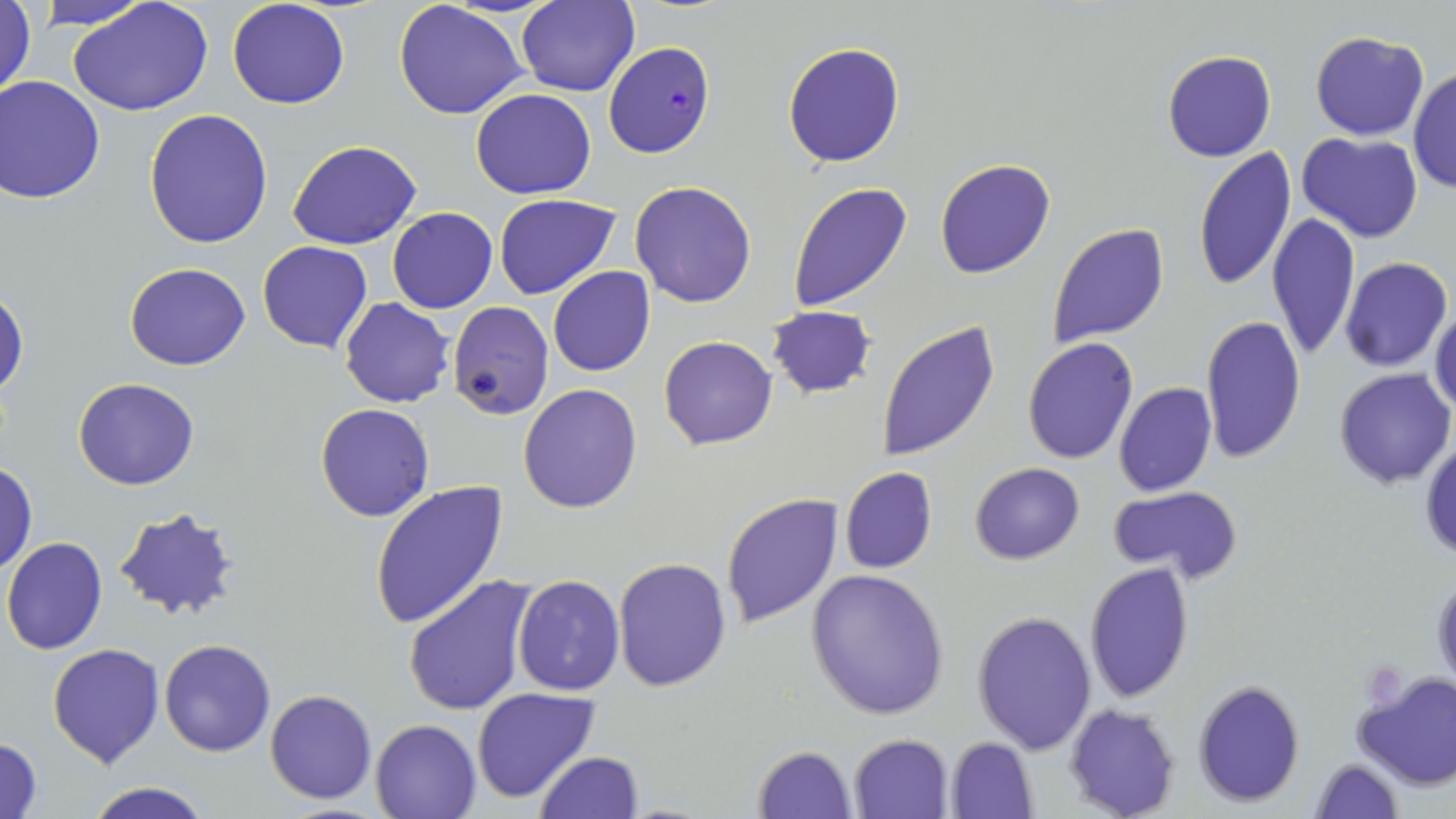
Summary:
  - Coordinate format: approximate bounding boxes as named x1/y1/x2/y2 corners in pixels
  - Uninfected red blood cell locations: (x1=29, y1=0, x2=155, y2=29), (x1=67, y1=1, x2=216, y2=117), (x1=226, y1=1, x2=351, y2=110), (x1=393, y1=1, x2=528, y2=120), (x1=515, y1=1, x2=638, y2=97), (x1=1, y1=2, x2=37, y2=103), (x1=1310, y1=31, x2=1427, y2=140), (x1=782, y1=42, x2=905, y2=167), (x1=1162, y1=50, x2=1276, y2=163), (x1=1410, y1=67, x2=1455, y2=195), (x1=0, y1=76, x2=106, y2=204), (x1=470, y1=88, x2=597, y2=199), (x1=142, y1=109, x2=274, y2=249), (x1=1297, y1=132, x2=1422, y2=241), (x1=289, y1=140, x2=421, y2=250), (x1=1193, y1=148, x2=1297, y2=292), (x1=935, y1=159, x2=1055, y2=279), (x1=629, y1=181, x2=757, y2=308), (x1=788, y1=182, x2=913, y2=314), (x1=494, y1=194, x2=620, y2=300), (x1=387, y1=207, x2=498, y2=313), (x1=1268, y1=212, x2=1360, y2=361), (x1=1047, y1=223, x2=1170, y2=348), (x1=256, y1=241, x2=373, y2=353), (x1=1339, y1=257, x2=1451, y2=372), (x1=125, y1=262, x2=251, y2=370), (x1=547, y1=265, x2=655, y2=377), (x1=0, y1=285, x2=26, y2=404), (x1=340, y1=297, x2=454, y2=408), (x1=765, y1=305, x2=878, y2=400), (x1=1429, y1=307, x2=1456, y2=416), (x1=1199, y1=316, x2=1307, y2=463), (x1=877, y1=321, x2=1002, y2=460), (x1=659, y1=335, x2=778, y2=450), (x1=1022, y1=336, x2=1139, y2=464), (x1=1334, y1=369, x2=1454, y2=489), (x1=74, y1=378, x2=200, y2=490), (x1=517, y1=383, x2=644, y2=515), (x1=1115, y1=383, x2=1217, y2=497), (x1=315, y1=403, x2=434, y2=521), (x1=1421, y1=436, x2=1456, y2=562), (x1=0, y1=460, x2=37, y2=576), (x1=970, y1=462, x2=1085, y2=563), (x1=840, y1=467, x2=937, y2=574), (x1=368, y1=479, x2=508, y2=630), (x1=1108, y1=486, x2=1245, y2=582), (x1=720, y1=493, x2=845, y2=631), (x1=113, y1=506, x2=244, y2=622), (x1=1, y1=537, x2=107, y2=655), (x1=612, y1=558, x2=732, y2=692), (x1=1083, y1=562, x2=1195, y2=704), (x1=805, y1=567, x2=952, y2=718), (x1=1432, y1=573, x2=1455, y2=694), (x1=403, y1=574, x2=537, y2=716), (x1=513, y1=575, x2=625, y2=695), (x1=972, y1=610, x2=1097, y2=754), (x1=158, y1=639, x2=276, y2=757), (x1=47, y1=643, x2=165, y2=767), (x1=1351, y1=668, x2=1456, y2=791), (x1=1192, y1=679, x2=1305, y2=808), (x1=471, y1=687, x2=600, y2=803), (x1=264, y1=688, x2=378, y2=805), (x1=1063, y1=703, x2=1183, y2=819), (x1=370, y1=718, x2=481, y2=819), (x1=848, y1=734, x2=956, y2=818), (x1=0, y1=737, x2=44, y2=818), (x1=946, y1=737, x2=1039, y2=817), (x1=753, y1=745, x2=857, y2=819), (x1=536, y1=751, x2=644, y2=819), (x1=1309, y1=759, x2=1404, y2=818), (x1=81, y1=781, x2=217, y2=819)
  - Plasmodium falciparum-infected red blood cell locations: (x1=603, y1=42, x2=716, y2=159), (x1=440, y1=304, x2=558, y2=422)
  - Slide-level diagnosis: Plasmodium falciparum
  - Stain: May-Grünwald-Giemsa
  - Image size: 1456×819 pixels
  - Modality: light microscopy
  - Magnification: 1000x
  - Preparation: thin blood smear
  - Field of view: single